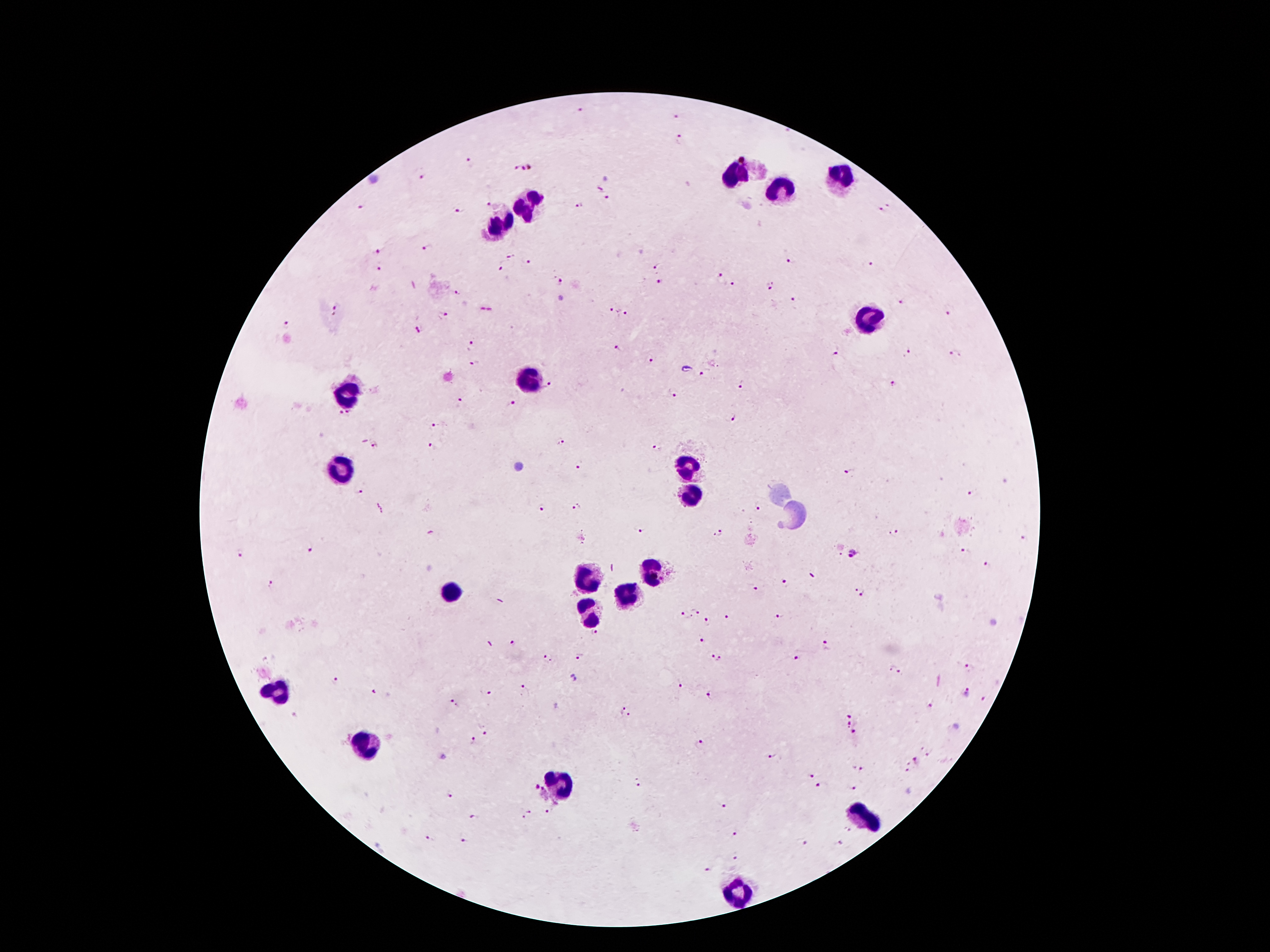

Approximate centers as (x, y) in pixels.
Summary:
  - Leukocyte locations: (738, 170), (838, 174), (778, 190), (529, 204), (501, 227), (869, 317), (527, 381), (349, 392), (685, 469), (343, 470), (692, 492), (654, 571), (588, 578), (450, 590), (624, 597), (586, 612), (279, 688), (372, 746), (558, 787), (865, 813), (736, 892)
  - Malaria parasite locations: (581, 110), (675, 117), (679, 140), (470, 161), (522, 168), (422, 177), (598, 189), (607, 200), (488, 202), (889, 204), (361, 206), (579, 207), (880, 209), (460, 211), (427, 248), (377, 251), (510, 256), (791, 258), (525, 262), (870, 264), (500, 265), (655, 265), (379, 269), (719, 274), (560, 281), (660, 281), (731, 283), (770, 284), (456, 293), (795, 300), (903, 303), (337, 308), (612, 310), (950, 311), (625, 313), (447, 314), (285, 324), (417, 329), (472, 345), (616, 349), (834, 349), (908, 353), (955, 355), (651, 360), (475, 364), (701, 374), (552, 384), (742, 384), (895, 385), (673, 393), (456, 399), (511, 404), (344, 416), (733, 420), (435, 423), (560, 442), (374, 445), (432, 447), (656, 448), (579, 468), (847, 471), (359, 491), (969, 493), (758, 505), (543, 508), (575, 508), (640, 529), (894, 532), (718, 534), (1024, 539), (310, 550), (241, 552), (853, 554), (964, 554), (988, 564), (786, 582), (271, 585), (755, 589), (862, 593), (695, 611), (685, 614), (780, 616), (726, 617), (705, 621), (595, 632), (702, 639), (514, 643), (827, 645), (715, 656), (580, 657), (798, 657), (548, 658), (969, 668), (897, 669), (336, 682), (680, 686), (526, 690), (968, 690), (374, 692), (489, 692), (709, 693), (984, 697), (454, 703), (930, 706), (627, 711), (851, 716), (847, 724), (487, 730), (854, 732), (473, 741), (700, 743), (927, 754), (770, 755), (917, 761), (859, 768), (813, 775), (640, 786), (818, 786), (536, 787), (852, 788), (449, 795), (725, 805), (547, 812), (474, 817), (527, 817), (848, 829), (735, 833), (426, 840), (462, 842), (804, 843), (840, 844), (737, 855), (706, 871)
  - Field of view: one from this slide
  - Capture: smartphone camera through the microscope eyepiece
  - Magnification: 100x
  - Patient malaria status: infected with Plasmodium falciparum
  - Stain: Giemsa
  - Preparation: thick peripheral-blood smear
  - Image size: 1270×952 pixels